Locate every malaria parasite.
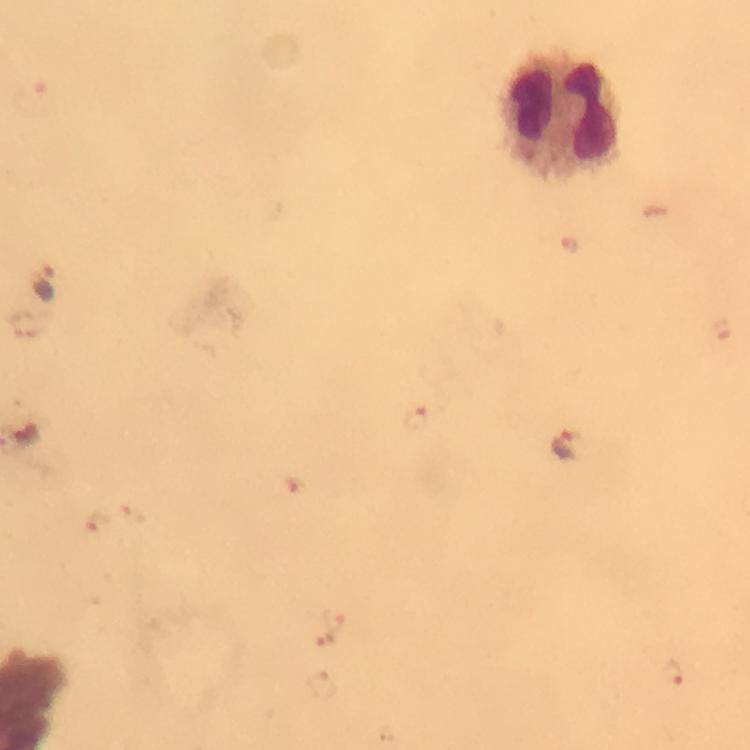
Approximate centers as (x, y) in pixels.
Malaria parasites: (571, 246), (47, 282), (415, 420), (565, 446), (333, 619), (324, 638), (671, 675).

Summary:
  - Leukocyte locations: (563, 118)
  - Magnification: 100x
  - Cropped from: a single field of view
  - Context: from a malaria diagnostic workup
  - Immersion oil: applied
  - Stain: Giemsa
  - Image size: 750×750 pixels
  - Capture: smartphone mounted on the microscope
  - Preparation: thick smear